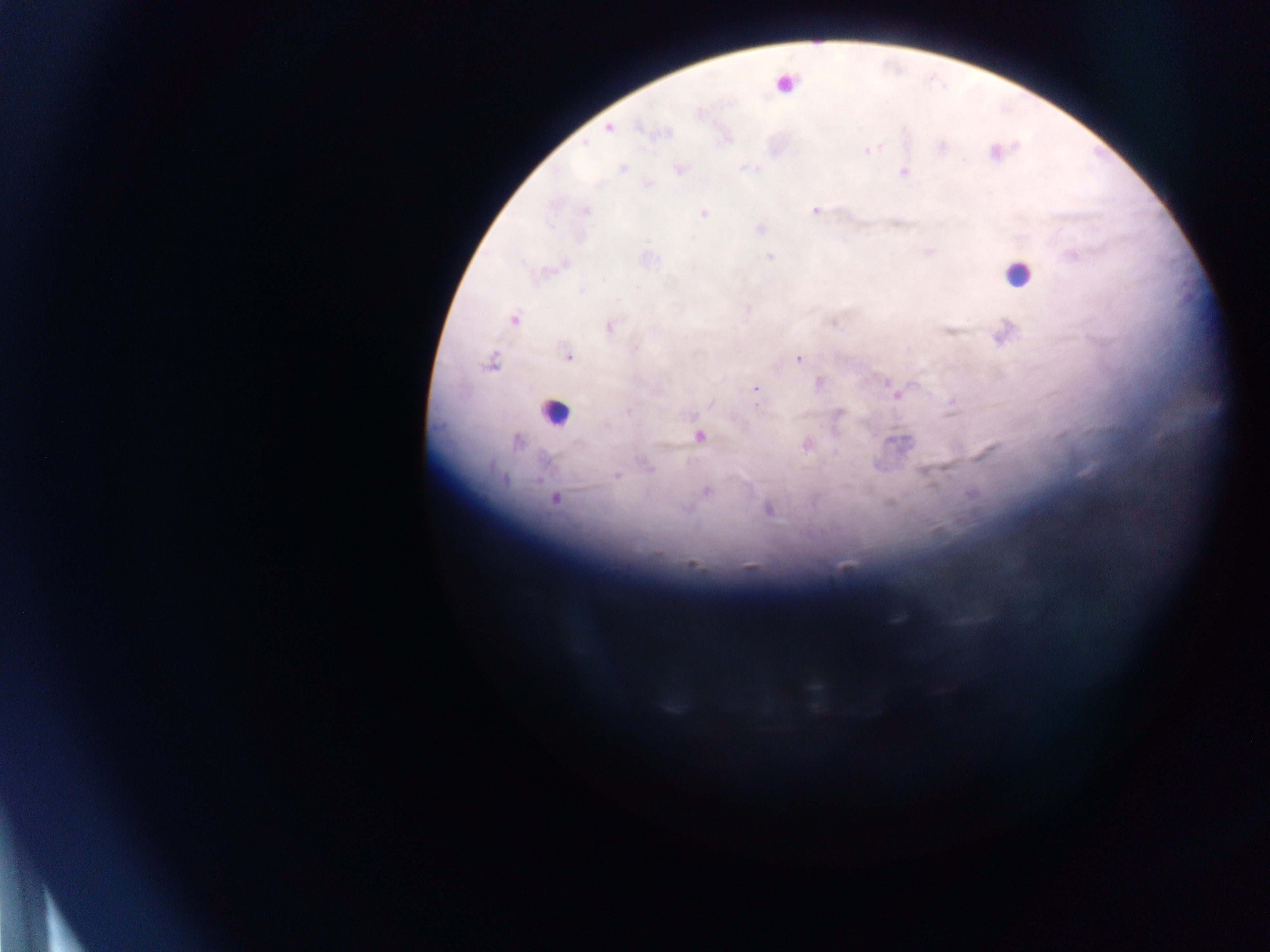
Approximate centers as (x, y) in pixels. Plasmodium parasite locations: (608, 128), (640, 128), (584, 144), (941, 147), (869, 150), (623, 168), (681, 168), (904, 172), (814, 210), (586, 211), (703, 214), (769, 256), (1072, 256), (564, 265), (604, 280), (617, 299), (748, 309), (513, 320), (608, 327), (634, 349), (568, 357), (798, 358), (490, 362), (820, 383), (755, 389), (895, 393), (710, 404), (629, 412), (839, 413), (607, 427), (699, 437), (517, 442), (649, 467), (616, 476), (504, 479), (706, 491), (555, 499), (767, 509), (692, 565). Leukocyte locations: (787, 81), (1017, 274), (555, 410). Photographed through a microscope with a mobile-phone camera. Image is 1270×952 pixels. Single field of view. Collected in Ghana. Thick blood film.